State which parasite is depicted.
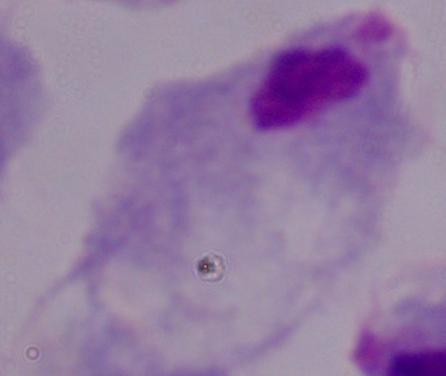

This is a trichomonad.

1000x magnification. Micrograph.